Locate every white blood cell.
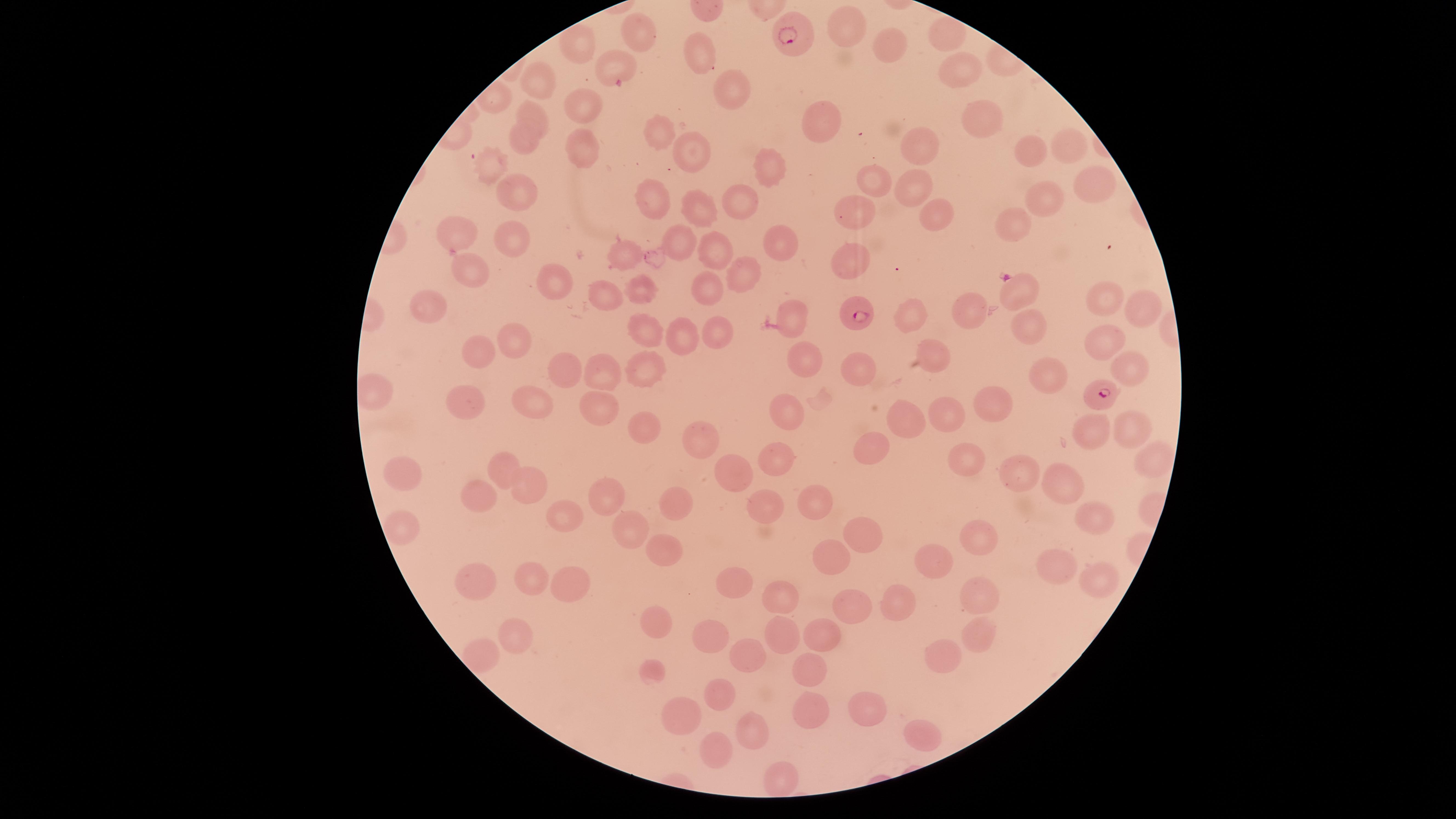

No white blood cells identified.

Approximate marker points, in pixels from the top-left corner.
Summary:
  - Uninfected red blood cells: (x=848, y=26), (x=945, y=33), (x=638, y=37), (x=582, y=41), (x=893, y=46), (x=699, y=50), (x=610, y=60), (x=965, y=66), (x=547, y=83), (x=735, y=89), (x=579, y=108), (x=530, y=113), (x=974, y=114), (x=818, y=117), (x=658, y=131), (x=524, y=140), (x=1058, y=141), (x=917, y=142), (x=582, y=147), (x=689, y=148), (x=1021, y=153), (x=772, y=166), (x=493, y=167), (x=1091, y=179), (x=876, y=182), (x=911, y=183), (x=518, y=188), (x=659, y=194), (x=1037, y=199), (x=738, y=202), (x=932, y=208), (x=700, y=210), (x=858, y=211), (x=1019, y=221), (x=456, y=229), (x=506, y=235), (x=681, y=241), (x=777, y=241), (x=624, y=253), (x=715, y=254), (x=858, y=261), (x=473, y=269), (x=746, y=274), (x=551, y=283), (x=639, y=285), (x=707, y=289), (x=606, y=298), (x=1104, y=298), (x=433, y=308), (x=969, y=308), (x=1140, y=310), (x=793, y=312), (x=913, y=316), (x=1023, y=326), (x=651, y=330), (x=720, y=332), (x=687, y=338), (x=509, y=341), (x=1099, y=343), (x=483, y=348), (x=934, y=351), (x=803, y=359), (x=561, y=366), (x=644, y=366), (x=858, y=366), (x=1125, y=367), (x=610, y=370), (x=1038, y=372), (x=526, y=396), (x=601, y=400), (x=988, y=400), (x=462, y=402), (x=791, y=413), (x=899, y=414), (x=956, y=414), (x=1131, y=421), (x=641, y=424), (x=1088, y=427), (x=706, y=434), (x=875, y=442), (x=777, y=452), (x=959, y=457), (x=1157, y=458), (x=506, y=462), (x=726, y=471), (x=395, y=472), (x=1024, y=473), (x=1054, y=480), (x=528, y=488), (x=478, y=490), (x=608, y=498), (x=669, y=500), (x=821, y=504), (x=769, y=506), (x=1087, y=509), (x=565, y=516), (x=400, y=523), (x=627, y=533), (x=979, y=535), (x=859, y=536), (x=666, y=549), (x=833, y=558), (x=938, y=559), (x=1060, y=568), (x=1099, y=574), (x=535, y=576), (x=478, y=577), (x=560, y=580), (x=733, y=582), (x=975, y=592), (x=784, y=598), (x=900, y=598), (x=857, y=603), (x=659, y=620), (x=514, y=624), (x=820, y=626), (x=986, y=630), (x=779, y=634), (x=720, y=637), (x=750, y=654), (x=481, y=655), (x=943, y=655), (x=808, y=669), (x=654, y=673), (x=719, y=690), (x=856, y=704), (x=805, y=707), (x=680, y=711), (x=746, y=729), (x=924, y=735), (x=715, y=752), (x=779, y=778)
  - Parasitized red blood cells: (x=789, y=37), (x=1017, y=288), (x=858, y=317), (x=1102, y=398)
  - Species: Plasmodium falciparum
  - Stain: Giemsa
  - Capture: smartphone photograph through the microscope eyepiece
  - Presence: malaria parasites detected
  - Field of view: single
  - Visible region: circular
  - Preparation: thin blood smear
  - Image size: 1456×819 pixels